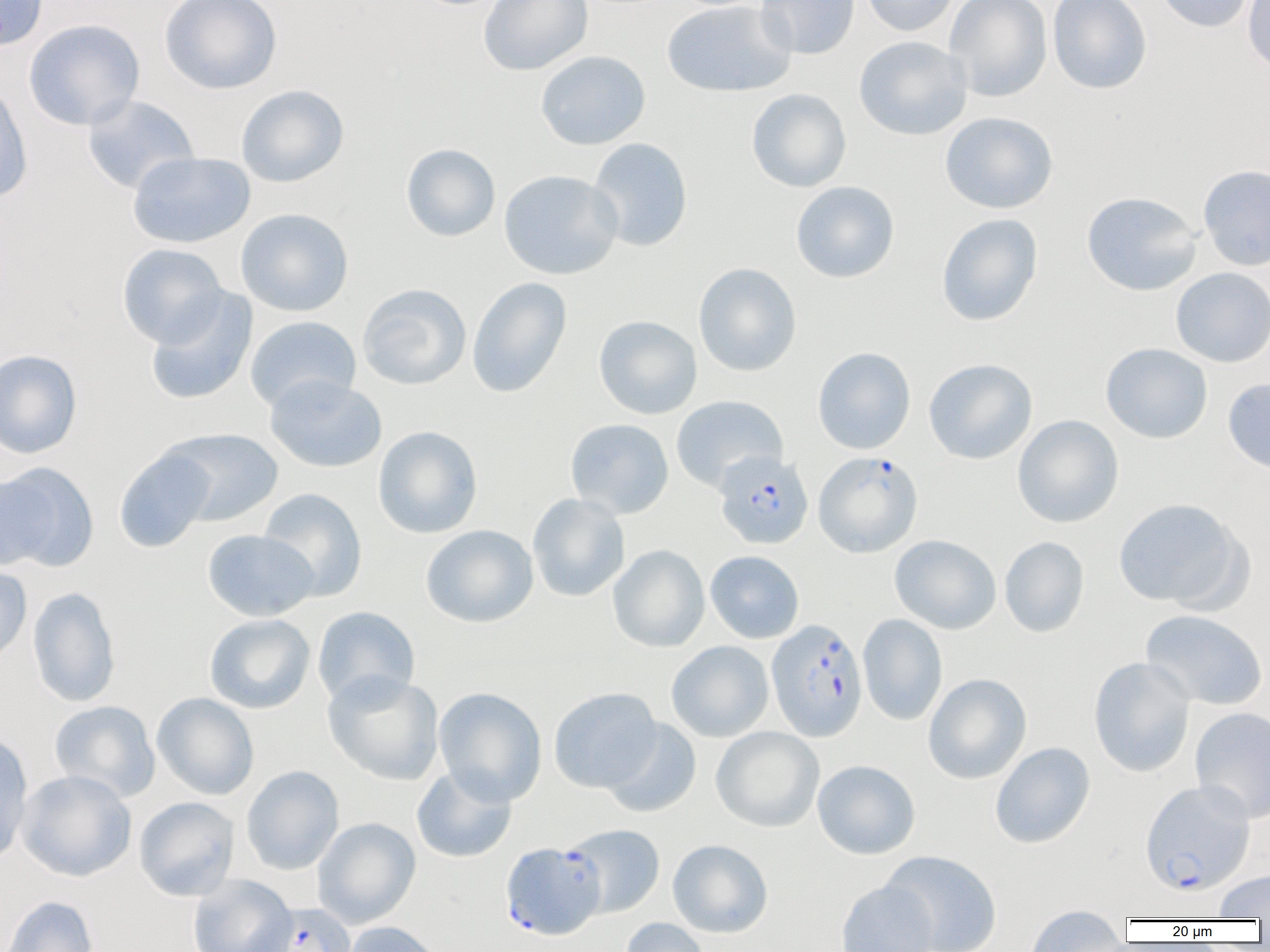

Approximate bounding boxes as [x1, y1, x2, y2] in pixels. Plasmodium falciparum-infected red blood cell locations: [813, 450, 923, 557], [714, 451, 814, 549], [766, 618, 868, 742], [1139, 779, 1256, 896], [561, 823, 665, 918], [500, 842, 605, 940], [251, 903, 357, 951]. Uninfected red blood cell locations: [0, 0, 49, 52], [159, 0, 282, 94], [479, 0, 593, 76], [756, 0, 860, 59], [859, 0, 960, 36], [944, 0, 1053, 102], [1047, 0, 1152, 94], [1154, 0, 1253, 33], [1242, 0, 1270, 74], [661, 1, 796, 97], [24, 19, 145, 131], [853, 36, 973, 140], [535, 50, 650, 150], [0, 82, 33, 204], [236, 84, 349, 188], [747, 88, 851, 193], [82, 95, 200, 194], [939, 111, 1058, 214], [588, 138, 693, 251], [401, 143, 500, 242], [127, 152, 255, 248], [1198, 165, 1270, 271], [498, 169, 623, 280], [790, 181, 900, 283], [1081, 191, 1202, 297], [235, 208, 354, 316], [936, 213, 1043, 327], [116, 243, 228, 347], [693, 263, 802, 377], [1170, 267, 1270, 368], [467, 276, 572, 398], [357, 283, 472, 390], [145, 288, 257, 405], [594, 315, 702, 419], [245, 316, 361, 413], [1101, 343, 1213, 443], [813, 347, 916, 454], [0, 349, 83, 459], [923, 358, 1037, 465], [265, 375, 387, 473], [1223, 378, 1270, 475], [671, 395, 788, 491], [1012, 415, 1124, 528], [565, 418, 674, 519], [373, 425, 483, 538], [161, 428, 283, 526], [113, 448, 217, 552], [1, 465, 99, 572], [258, 487, 367, 602], [527, 493, 630, 602], [1112, 497, 1248, 611], [421, 524, 538, 628], [202, 529, 319, 621], [889, 534, 1001, 634], [1000, 536, 1089, 638], [608, 544, 710, 652], [705, 550, 804, 643], [0, 564, 32, 667], [27, 586, 121, 707], [312, 606, 420, 707], [1141, 609, 1268, 710], [204, 614, 316, 714], [858, 614, 947, 726], [666, 640, 774, 742], [1088, 656, 1196, 777], [323, 670, 445, 786], [923, 673, 1031, 784], [433, 687, 548, 807], [549, 687, 661, 793], [152, 693, 259, 800], [49, 700, 160, 802], [1190, 706, 1270, 824], [600, 718, 702, 818], [711, 726, 824, 832], [0, 731, 34, 867], [990, 742, 1095, 848], [812, 760, 920, 859], [241, 765, 344, 875], [411, 765, 517, 863], [16, 770, 137, 881], [134, 796, 240, 901], [313, 817, 420, 927], [667, 839, 773, 937], [880, 849, 1002, 952], [1213, 868, 1270, 919], [188, 874, 297, 952], [836, 879, 938, 952], [1, 895, 100, 952], [1024, 905, 1129, 951], [620, 918, 710, 952], [342, 921, 445, 952]. Slide-level diagnosis: Plasmodium falciparum. Light microscopy. Image is 1270×952 pixels. Single field of view. Captured at 1000x magnification. Thin blood film.